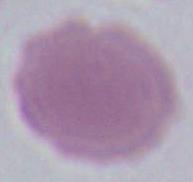
magnification = 1000x
modality = photomicrograph
identification = red blood cell